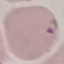

Summary:
  - Malaria status: parasitized
  - Capture: smartphone camera at the microscope eyepiece
  - Image type: cell patch, automatically extracted from a larger field of view and resized to 64 × 64 pixels
  - Stain: Giemsa
  - Preparation: thin blood smear